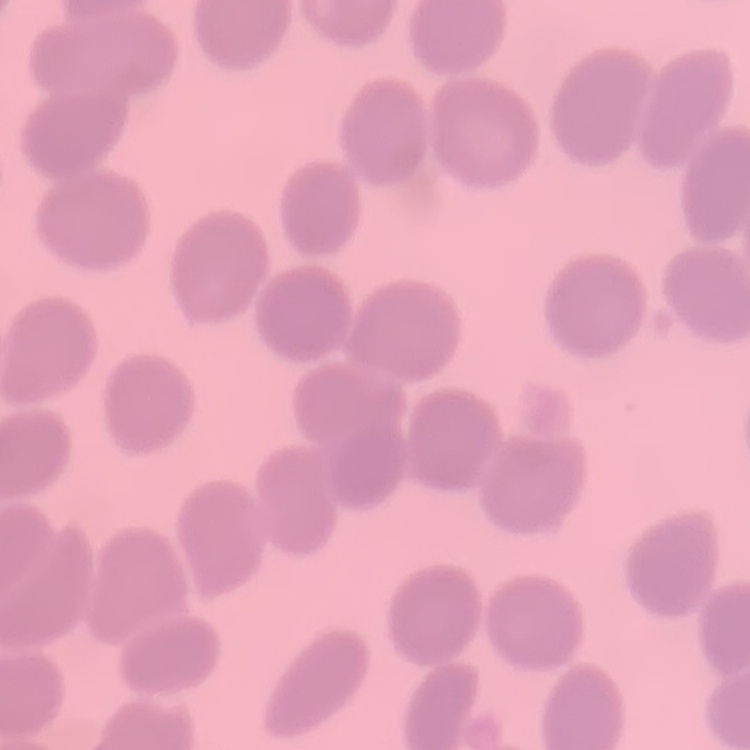
Summary:
  - Red blood cell morphology: no rouleaux formation
  - Preparation: thin peripheral smear
  - Stain: Field's or Giemsa
  - Image type: one tile cut from a larger photomicrograph